Give the extent of all Plasmodium ovale-infected red blood cells.
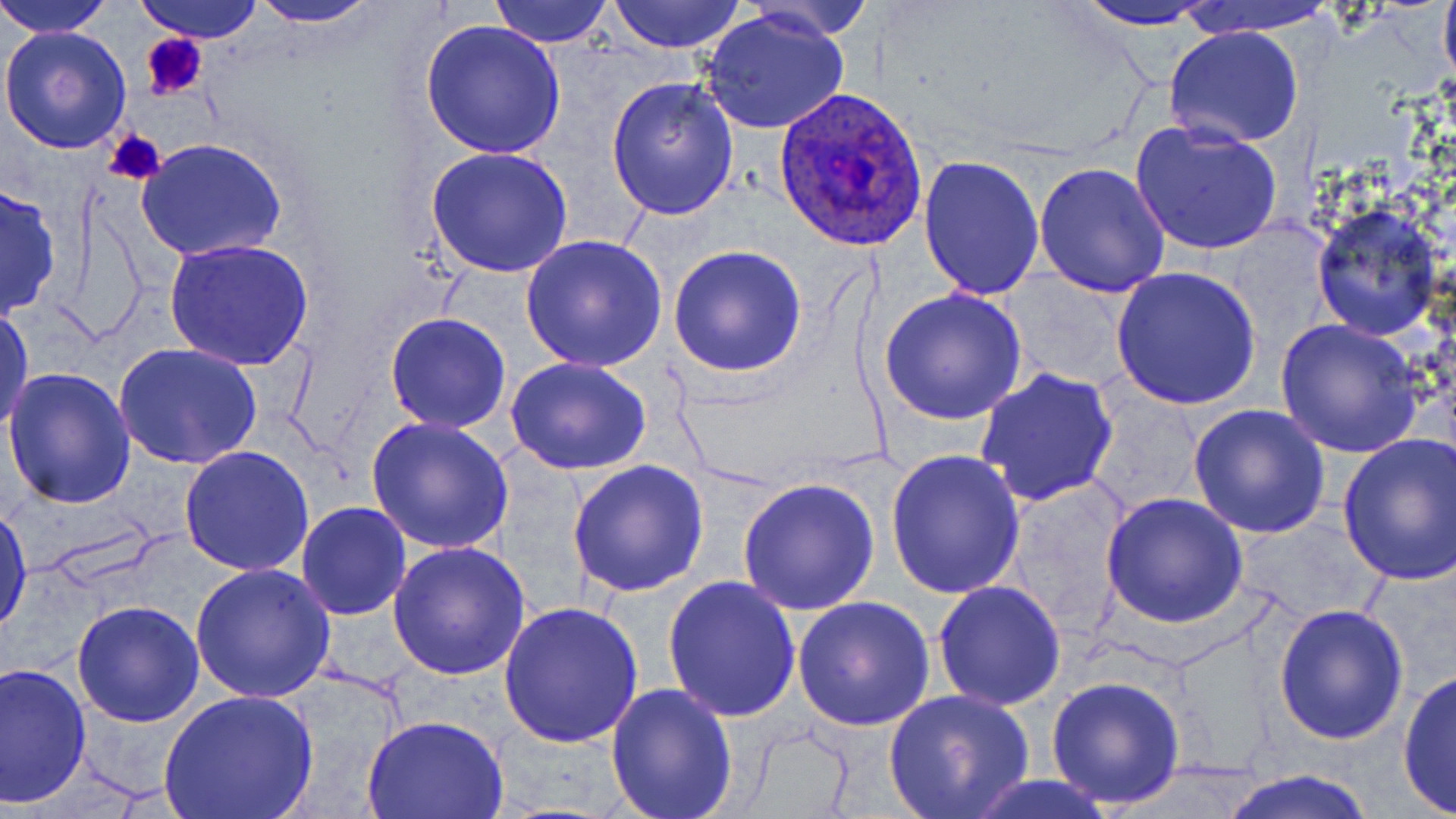

Approximate bounding boxes as (x1,y1)-(x2,y2) corner pairs in pixels.
Plasmodium ovale-infected red blood cells: (774,88)-(930,250).

slide-level diagnosis = Plasmodium ovale
field of view = single
image size = 1456×819 pixels
stain = May-Grünwald-Giemsa
magnification = 1000x
modality = light microscopy
preparation = thin blood film
uninfected red blood cell locations = approximate bounding boxes as (x1,y1)-(x2,y2) corner pairs in pixels: (0,0)-(116,38), (136,0)-(263,42), (244,0)-(383,27), (488,0)-(615,48), (606,0)-(748,53), (739,0)-(876,41), (1067,0)-(1222,30), (1179,0)-(1336,36), (1439,0)-(1456,94), (702,9)-(851,136), (420,19)-(566,159), (0,25)-(133,155), (1163,25)-(1306,150), (606,75)-(740,219), (1132,118)-(1285,255), (135,137)-(287,262), (425,148)-(573,280), (919,155)-(1045,300), (1033,163)-(1172,299), (0,179)-(62,322), (1310,207)-(1441,341), (521,236)-(668,373), (165,238)-(314,372), (668,244)-(807,377), (1110,266)-(1262,412), (999,274)-(1137,388), (879,289)-(1028,427), (0,302)-(35,443), (384,312)-(511,433), (1274,318)-(1425,458), (115,342)-(263,468), (507,356)-(654,475), (974,367)-(1118,507), (3,368)-(136,508), (1188,404)-(1332,539), (367,417)-(515,556), (1335,434)-(1456,585), (179,446)-(315,575), (883,449)-(1026,598), (567,460)-(709,598), (736,476)-(881,616), (1005,479)-(1139,630), (1101,493)-(1249,629), (1,501)-(32,636), (296,502)-(412,621), (386,541)-(531,679), (191,564)-(337,703), (663,576)-(801,723), (933,580)-(1067,712), (791,593)-(936,731), (497,599)-(643,747), (72,600)-(205,727), (1273,602)-(1409,744), (1,661)-(92,805), (1398,667)-(1455,815), (1045,676)-(1186,810), (605,681)-(739,817), (157,688)-(320,819), (883,689)-(1035,818), (363,715)-(508,819), (1216,769)-(1381,819), (958,773)-(1118,818)
platelet locations = approximate bounding boxes as (x1,y1)-(x2,y2) corner pairs in pixels: (139,33)-(208,100), (103,129)-(164,188)